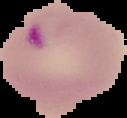
image size = 127×118 pixels
image type = segmented cell region with the area outside set to black
malaria status = parasitized
preparation = thin blood smear